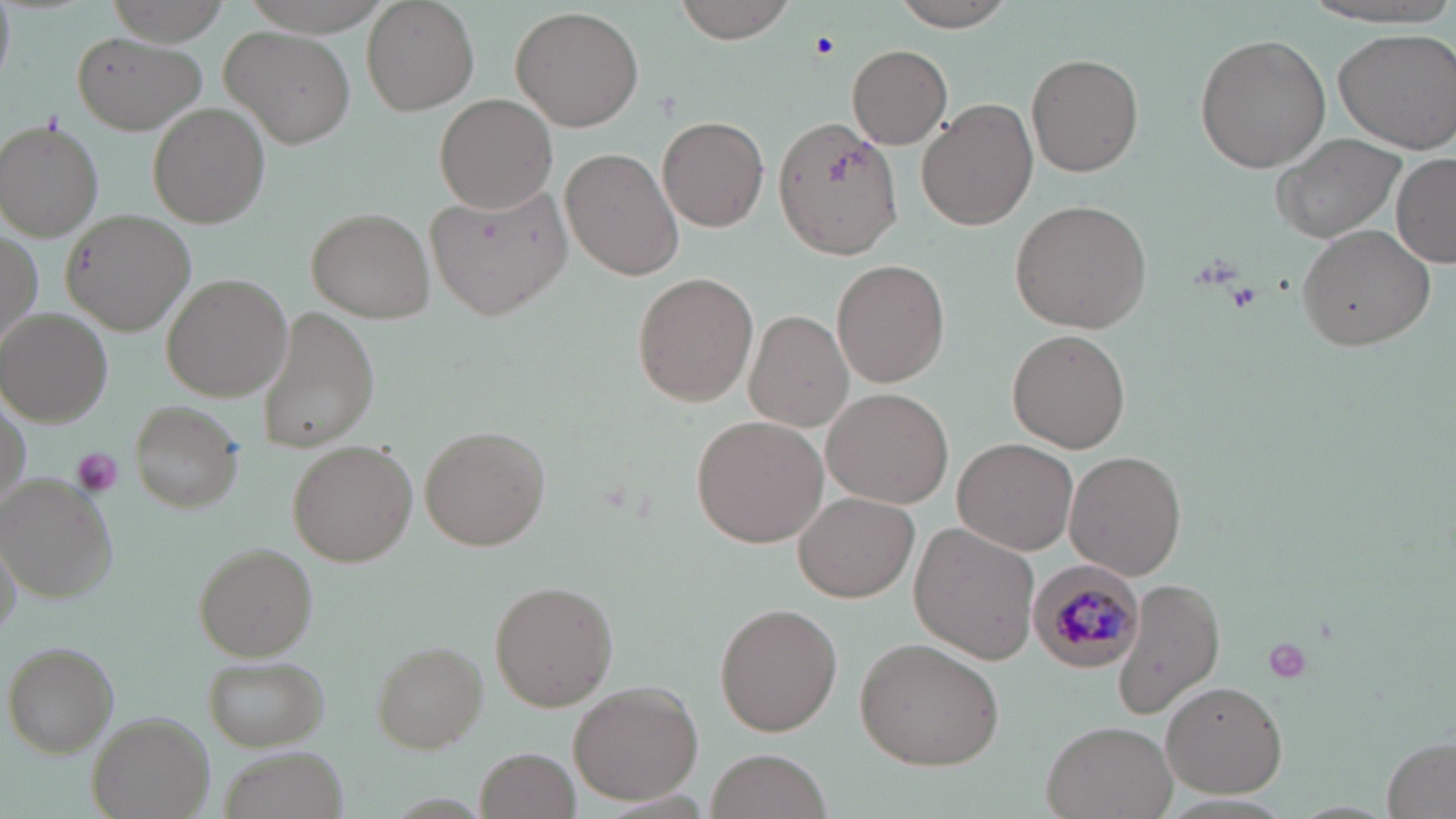

Summary:
  - Coordinate format: approximate bounding boxes as (x1,y1)-(x2,y2) corner pairs in pixels
  - Plasmodium malariae-infected red blood cell locations: (1027,559)-(1143,673)
  - Uninfected red blood cell locations: (362,0)-(479,115), (674,0)-(801,44), (894,0)-(1019,30), (512,6)-(644,132), (220,26)-(355,150), (1331,27)-(1456,153), (72,32)-(205,134), (1195,33)-(1331,174), (848,43)-(952,149), (1026,53)-(1143,176), (434,93)-(557,213), (916,100)-(1039,230), (149,103)-(269,226), (658,115)-(769,231), (773,118)-(905,261), (0,119)-(105,241), (1268,132)-(1408,244), (562,148)-(684,282), (1392,154)-(1456,267), (427,182)-(570,319), (1011,200)-(1152,333), (308,207)-(436,324), (62,209)-(194,335), (1295,224)-(1436,353), (833,259)-(949,389), (162,272)-(294,402), (633,272)-(759,406), (256,309)-(378,453), (3,310)-(113,425), (743,310)-(856,433), (1005,329)-(1133,452), (820,386)-(954,509), (2,395)-(30,510), (130,400)-(246,511), (691,414)-(829,548), (421,425)-(548,551), (952,437)-(1078,556), (288,440)-(418,568), (1065,451)-(1186,580), (0,473)-(114,600), (794,491)-(919,602), (909,524)-(1040,665), (2,535)-(21,638), (194,543)-(320,660), (1113,577)-(1225,721), (492,580)-(618,711), (715,603)-(842,736), (853,637)-(1006,771), (5,640)-(118,757), (374,641)-(487,752), (203,655)-(328,750), (568,680)-(704,804), (1160,680)-(1289,799), (90,712)-(215,819), (1042,720)-(1179,819), (1382,738)-(1455,817), (476,748)-(580,819), (222,749)-(344,819), (705,750)-(834,819)
  - Platelet locations: (809,32)-(837,61), (1223,280)-(1262,313), (68,445)-(123,499), (1261,635)-(1315,686)
  - Slide-level diagnosis: Plasmodium malariae
  - Modality: optical microscopy
  - Field of view: single
  - Image size: 1456×819 pixels
  - Preparation: thin blood film
  - Magnification: 1000x
  - Stain: May-Grünwald-Giemsa